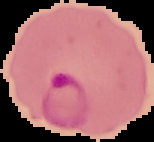 From a thin blood smear. Malaria status: parasitized. Cell region segmented out of the field of view; the surrounding area is masked to black. Image is 154×142 pixels.